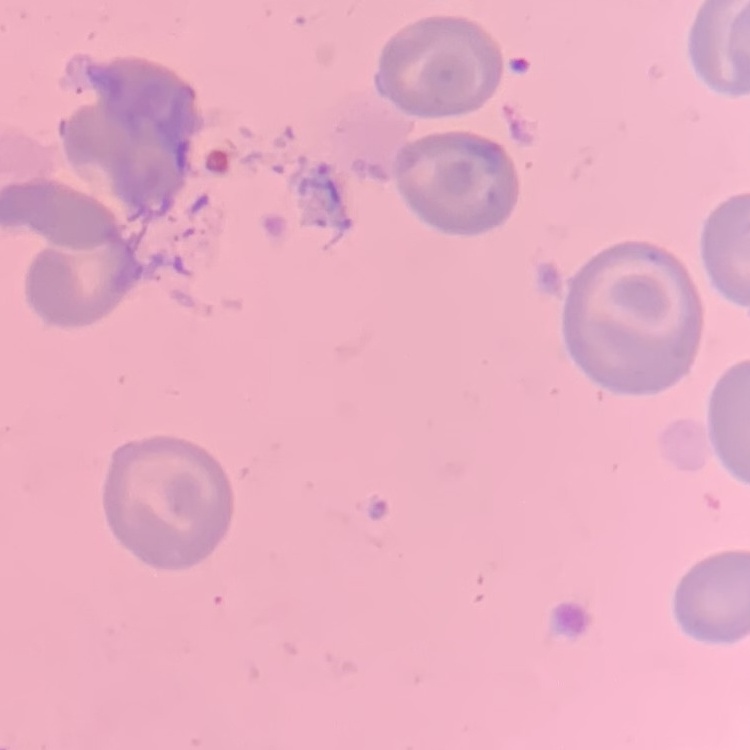

Summary:
  - Red blood cell morphology: no rouleaux formation
  - Stain: Field's or Giemsa
  - Image type: square crop of a larger photomicrograph
  - Preparation: thin peripheral smear